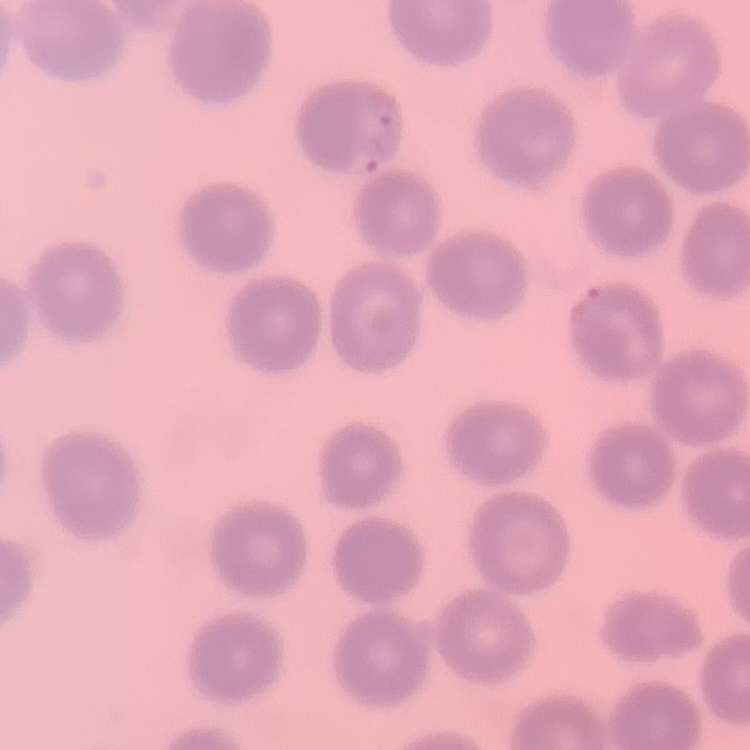

{
  "red_blood_cell_morphology": "no rouleaux formation",
  "preparation": "thin blood smear",
  "image_type": "one tile cut from a larger photomicrograph",
  "stain": "Field's or Giemsa"
}